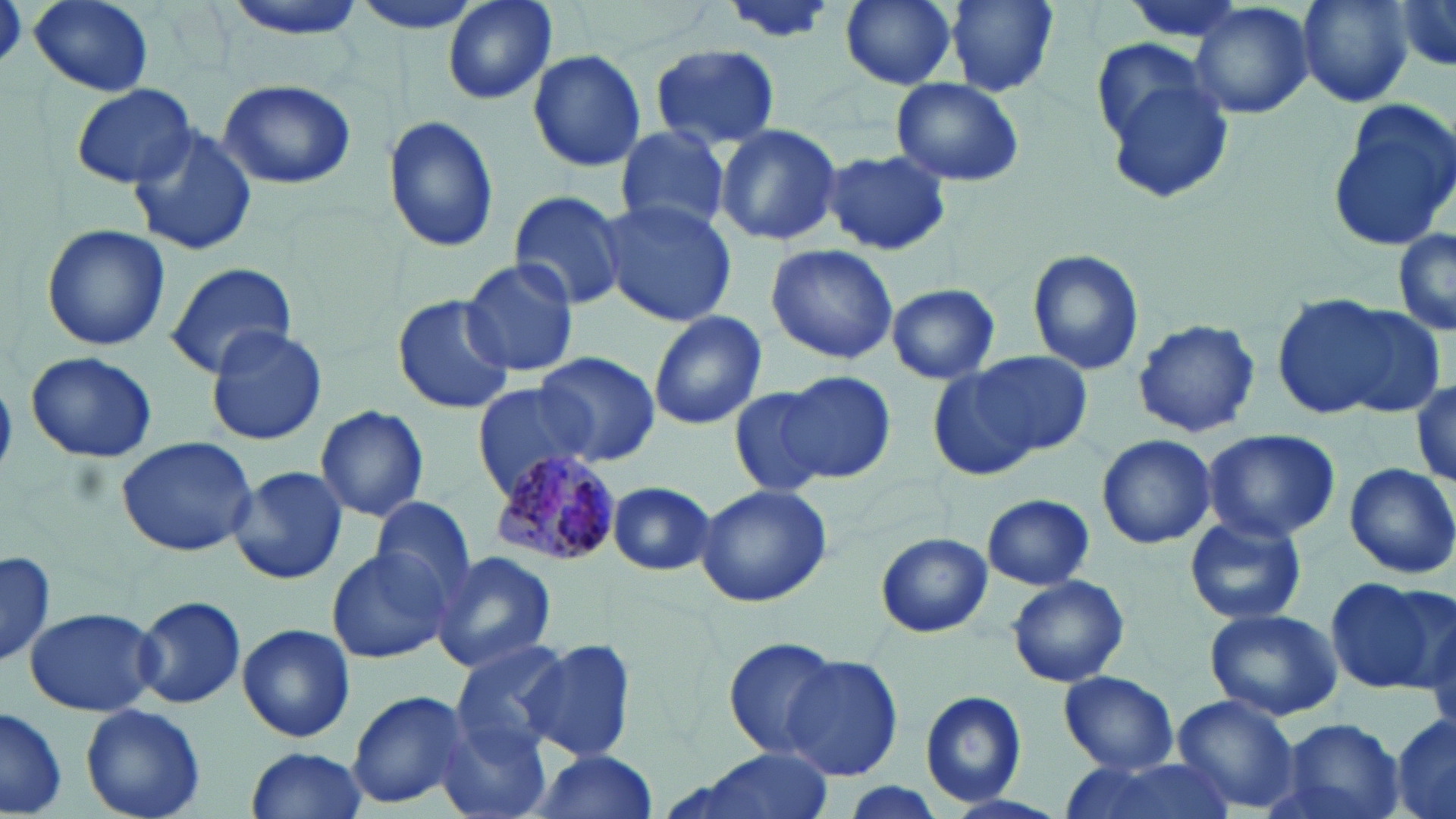
Summary:
  - Coordinate format: approximate bounding boxes as (x1, y1, x2, y2) in pixels
  - Uninfected red blood cell locations: (29, 0, 155, 94), (220, 0, 373, 38), (444, 0, 556, 106), (716, 0, 840, 47), (839, 0, 959, 89), (948, 0, 1060, 96), (1294, 0, 1414, 107), (1394, 0, 1456, 78), (1189, 2, 1315, 120), (648, 43, 784, 150), (526, 50, 647, 173), (1097, 60, 1236, 208), (887, 75, 1026, 187), (217, 77, 357, 189), (72, 83, 195, 187), (1327, 99, 1456, 254), (383, 115, 500, 252), (614, 123, 733, 236), (715, 124, 842, 246), (128, 126, 259, 256), (820, 149, 952, 256), (508, 189, 628, 311), (598, 200, 737, 325), (41, 224, 171, 352), (1392, 226, 1456, 339), (764, 242, 899, 365), (1026, 249, 1145, 376), (463, 257, 583, 380), (163, 262, 298, 380), (885, 283, 1002, 384), (391, 294, 517, 415), (1269, 294, 1413, 421), (1329, 300, 1448, 421), (646, 310, 768, 430), (1131, 317, 1260, 438), (204, 324, 328, 446), (25, 351, 156, 463), (971, 352, 1093, 458), (535, 353, 660, 463), (929, 360, 1057, 481), (778, 368, 896, 484), (1411, 378, 1456, 489), (472, 382, 594, 494), (727, 384, 843, 498), (315, 406, 430, 522), (1199, 429, 1343, 543), (1096, 433, 1217, 550), (116, 435, 258, 557), (1345, 462, 1456, 578), (227, 468, 351, 587), (606, 480, 716, 576), (694, 482, 834, 608), (981, 494, 1093, 590), (369, 496, 475, 604), (1184, 514, 1308, 626), (876, 532, 991, 638), (327, 546, 457, 663), (1, 549, 54, 670), (431, 551, 557, 672), (1006, 575, 1130, 687), (1326, 575, 1451, 693), (135, 595, 248, 711), (1422, 599, 1456, 739), (24, 606, 160, 716), (1202, 607, 1342, 720), (237, 623, 356, 744), (719, 636, 842, 759), (518, 639, 636, 763), (449, 641, 574, 746), (782, 655, 903, 780), (1059, 671, 1177, 774), (345, 688, 475, 812), (919, 690, 1028, 808), (1171, 692, 1302, 814), (80, 703, 207, 819), (0, 704, 68, 816), (1392, 711, 1456, 819), (439, 715, 553, 819), (1272, 716, 1405, 819), (243, 747, 369, 819), (694, 748, 833, 819), (524, 750, 660, 819), (1059, 754, 1230, 819)
  - Plasmodium malariae-infected red blood cell locations: (485, 449, 626, 569)
  - Slide-level diagnosis: Plasmodium malariae
  - Preparation: thin blood film
  - Stain: May-Grünwald-Giemsa
  - Field of view: single
  - Modality: optical microscopy
  - Image size: 1456×819 pixels
  - Magnification: 1000x